Point out each malaria parasite and each leukocyte.
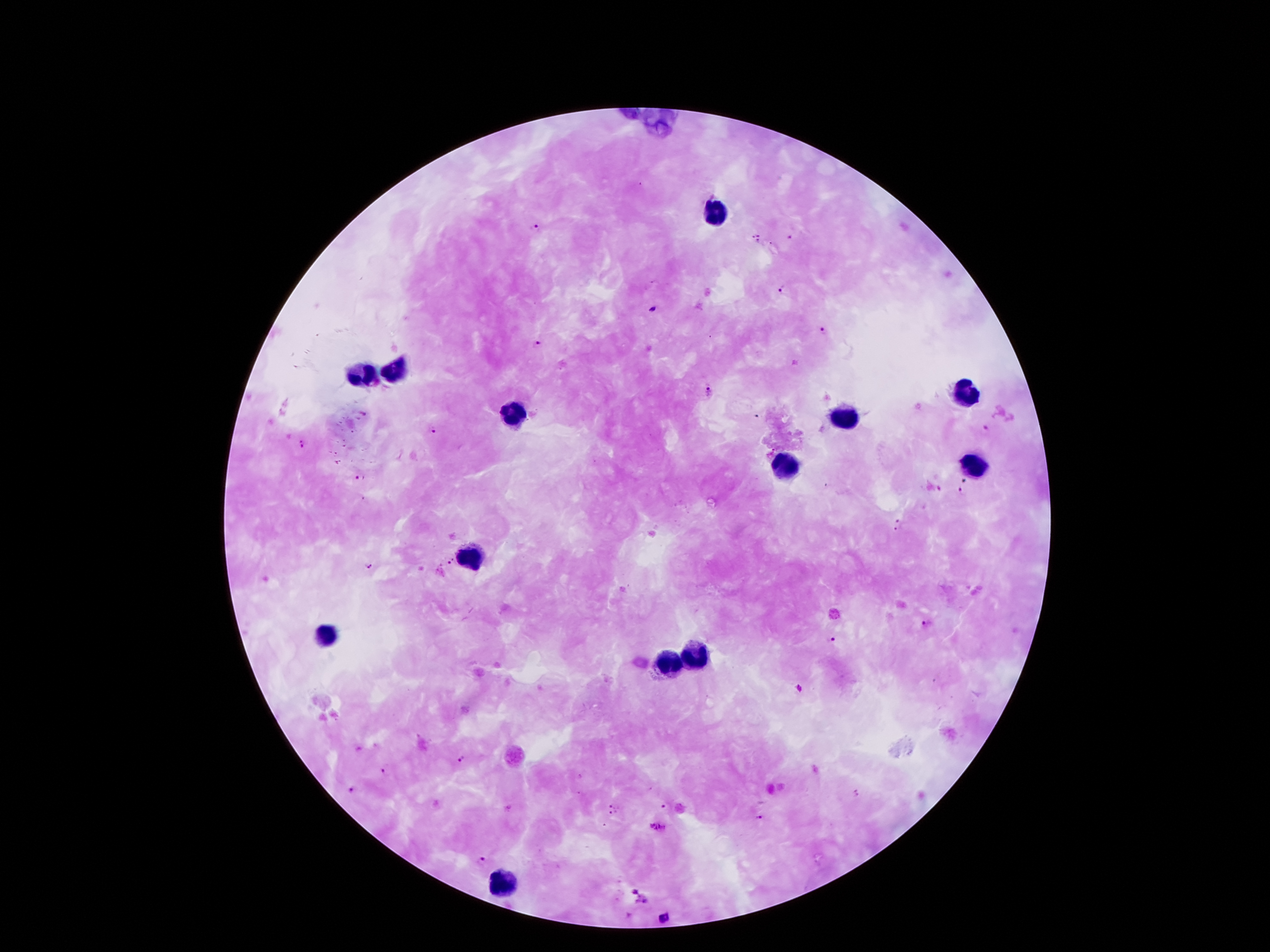

Approximate object centers, in pixels from the top-left corner.
Malaria parasites: (x=535, y=229), (x=791, y=238), (x=755, y=239), (x=785, y=293), (x=654, y=310), (x=824, y=330), (x=538, y=344), (x=707, y=391), (x=758, y=416), (x=988, y=427), (x=435, y=432), (x=303, y=446), (x=363, y=477), (x=966, y=480), (x=961, y=494), (x=898, y=526), (x=448, y=562), (x=370, y=566), (x=924, y=621), (x=832, y=639), (x=800, y=688), (x=464, y=757), (x=387, y=769), (x=351, y=789), (x=856, y=794), (x=665, y=804), (x=613, y=808), (x=759, y=818), (x=480, y=859), (x=665, y=917).
Leukocytes: (x=716, y=211), (x=394, y=371), (x=364, y=375), (x=962, y=397), (x=513, y=416), (x=841, y=416), (x=974, y=465), (x=786, y=471), (x=468, y=557), (x=323, y=631), (x=700, y=654), (x=667, y=666), (x=499, y=885).

{
  "capture": "smartphone through the microscope eyepiece",
  "preparation": "thick blood film",
  "patient_malaria_status": "infected with Plasmodium falciparum",
  "stain": "Giemsa",
  "field_of_view": "single",
  "image_size": "1270×952 pixels",
  "magnification": "100x"
}